Give the position of every Plasmodium parasite.
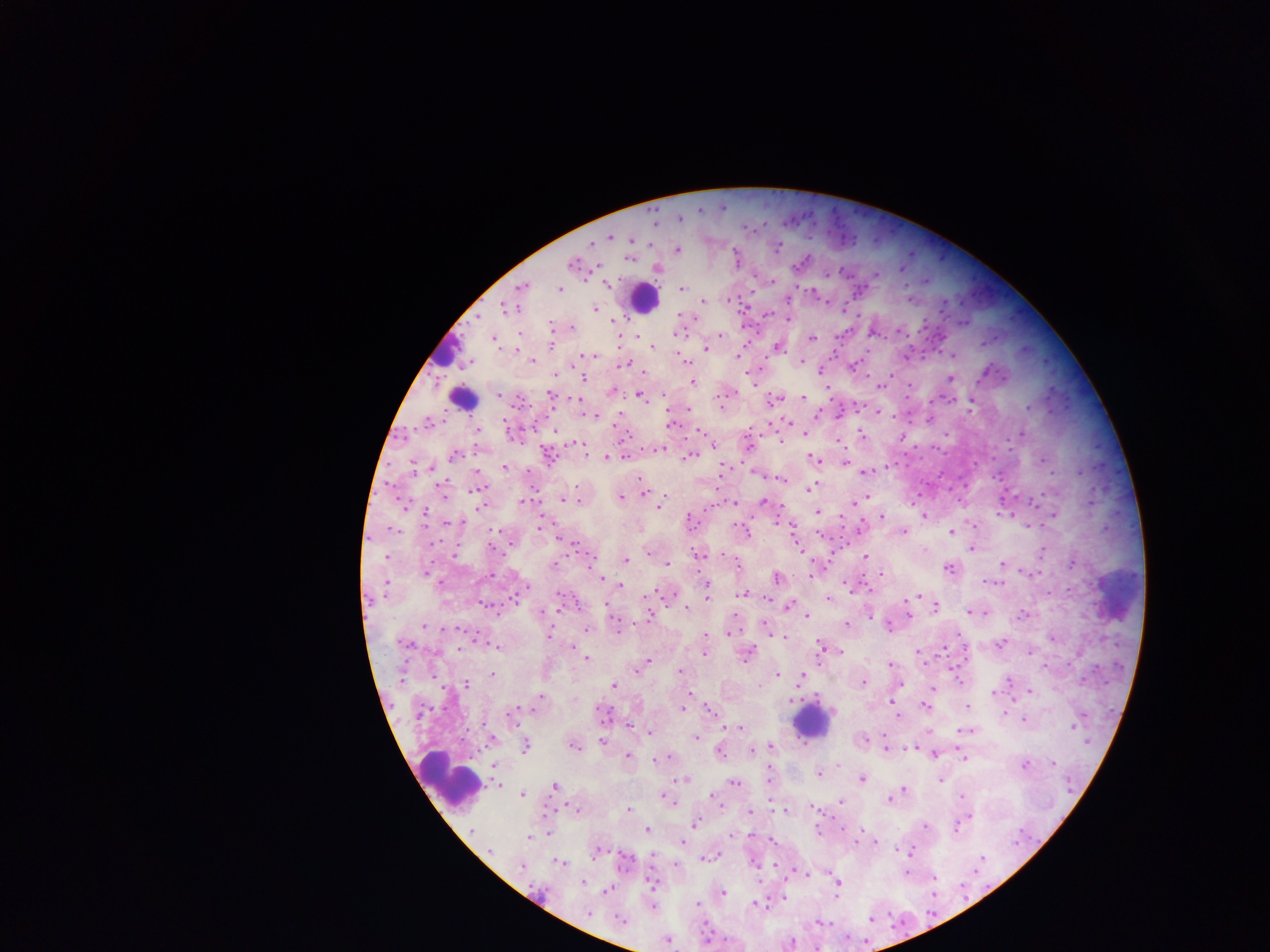
Approximate centers as [x, y] in pixels.
Plasmodium parasites: [752, 228], [611, 238], [633, 241], [651, 244], [778, 248], [678, 250], [631, 257], [737, 257], [804, 262], [902, 270], [828, 275], [877, 275], [927, 282], [608, 285], [683, 289], [561, 291], [910, 297], [704, 302], [596, 311], [680, 315], [614, 320], [552, 327], [572, 328], [520, 335], [637, 337], [721, 337], [813, 339], [620, 340], [496, 342], [654, 347], [517, 349], [707, 350], [953, 355], [594, 356], [739, 357], [685, 360], [533, 361], [626, 365], [822, 373], [556, 375], [951, 379], [694, 382], [754, 383], [882, 386], [613, 392], [499, 396], [551, 397], [642, 397], [804, 397], [775, 401], [972, 403], [723, 407], [688, 409], [878, 413], [586, 415], [817, 415], [594, 418], [672, 424], [806, 434], [863, 436], [903, 438], [839, 440], [782, 441], [750, 446], [661, 450], [455, 456], [626, 457], [691, 458], [812, 458], [606, 459], [816, 460], [846, 462], [505, 468], [725, 470], [477, 471], [865, 472], [782, 477], [640, 480], [810, 489], [644, 493], [445, 496], [622, 498], [564, 501], [524, 502], [581, 502], [763, 502], [732, 503], [855, 503], [659, 507], [483, 508], [818, 512], [882, 517], [924, 517], [1054, 517], [691, 522], [447, 523], [777, 523], [540, 527], [974, 527], [1030, 527], [861, 530], [793, 531], [952, 532], [746, 533], [905, 533], [573, 545], [491, 548], [974, 549], [1045, 551], [648, 554], [700, 555], [455, 557], [387, 558], [866, 558], [627, 561], [1003, 564], [555, 565], [668, 565], [1072, 565], [950, 569], [426, 574], [1031, 574], [493, 575], [812, 575], [882, 576], [778, 579], [603, 580], [994, 584], [621, 586], [707, 588], [528, 589], [744, 595], [708, 596], [917, 598], [768, 599], [830, 600], [914, 602], [790, 607], [687, 608], [936, 609], [558, 610], [970, 613], [985, 613], [807, 615], [910, 615], [1024, 616], [651, 617], [871, 617], [848, 625], [424, 627], [890, 627], [767, 628], [588, 631], [770, 631], [730, 634], [550, 635], [959, 635], [707, 636], [782, 639], [1053, 639], [1002, 644], [408, 645], [822, 647], [497, 648], [459, 650], [944, 650], [840, 652], [918, 653], [706, 654], [749, 654], [1031, 654], [587, 660], [649, 662], [644, 665], [891, 665], [1044, 667], [639, 670], [681, 672], [492, 675], [778, 676], [803, 676], [959, 680], [1010, 680], [402, 682], [864, 684], [466, 686], [899, 686], [615, 687], [933, 688], [1031, 692], [994, 693], [689, 695], [542, 697], [793, 701], [894, 703], [925, 706], [968, 708], [535, 710], [683, 710], [710, 710], [514, 714], [1006, 714], [421, 715], [897, 715], [605, 716], [1024, 720], [629, 726], [1073, 727], [742, 728], [966, 732], [650, 734], [698, 739], [492, 741], [865, 741], [602, 742], [1087, 744], [526, 748], [770, 748], [574, 749], [886, 749], [914, 749], [753, 751], [720, 754], [936, 755], [628, 757], [965, 757], [669, 758], [655, 761], [1054, 764], [839, 765], [1026, 766], [497, 767], [819, 775], [770, 777], [686, 780], [863, 780], [942, 781], [736, 784], [1069, 786], [555, 787], [500, 788], [904, 791], [901, 794], [523, 796], [663, 797], [962, 797], [670, 800], [716, 800], [891, 800], [842, 802], [721, 804], [815, 809], [629, 810], [577, 812], [785, 812], [750, 813], [970, 817], [697, 824], [926, 827], [958, 830], [472, 831], [648, 831], [818, 832], [549, 833], [859, 835], [733, 836], [750, 836], [529, 838], [772, 841], [875, 842], [1019, 842], [684, 844], [491, 852], [911, 852], [598, 853], [653, 856], [711, 858], [982, 860], [626, 862], [562, 864], [756, 865], [675, 866], [524, 868], [807, 875], [907, 875], [936, 879], [584, 883], [652, 884], [838, 888], [963, 890], [608, 892], [934, 893], [543, 894], [724, 895], [784, 899], [699, 905], [756, 905], [655, 909], [590, 914], [872, 921], [623, 922], [820, 924], [848, 939], [708, 940], [668, 942], [793, 944].

Summary:
  - Leukocyte locations: [644, 300], [442, 353], [460, 401], [1117, 595], [811, 723], [450, 782]
  - Country: Ghana
  - Image size: 1270×952 pixels
  - Preparation: thick blood film
  - Field of view: single
  - Capture: mobile-phone photograph through a microscope